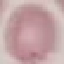
malaria status = uninfected
preparation = thin smear
stain = Giemsa
image type = cell patch, automatically extracted from a larger field of view and resized to 64 × 64 pixels
capture = smartphone camera at the microscope eyepiece